Report the malaria status.
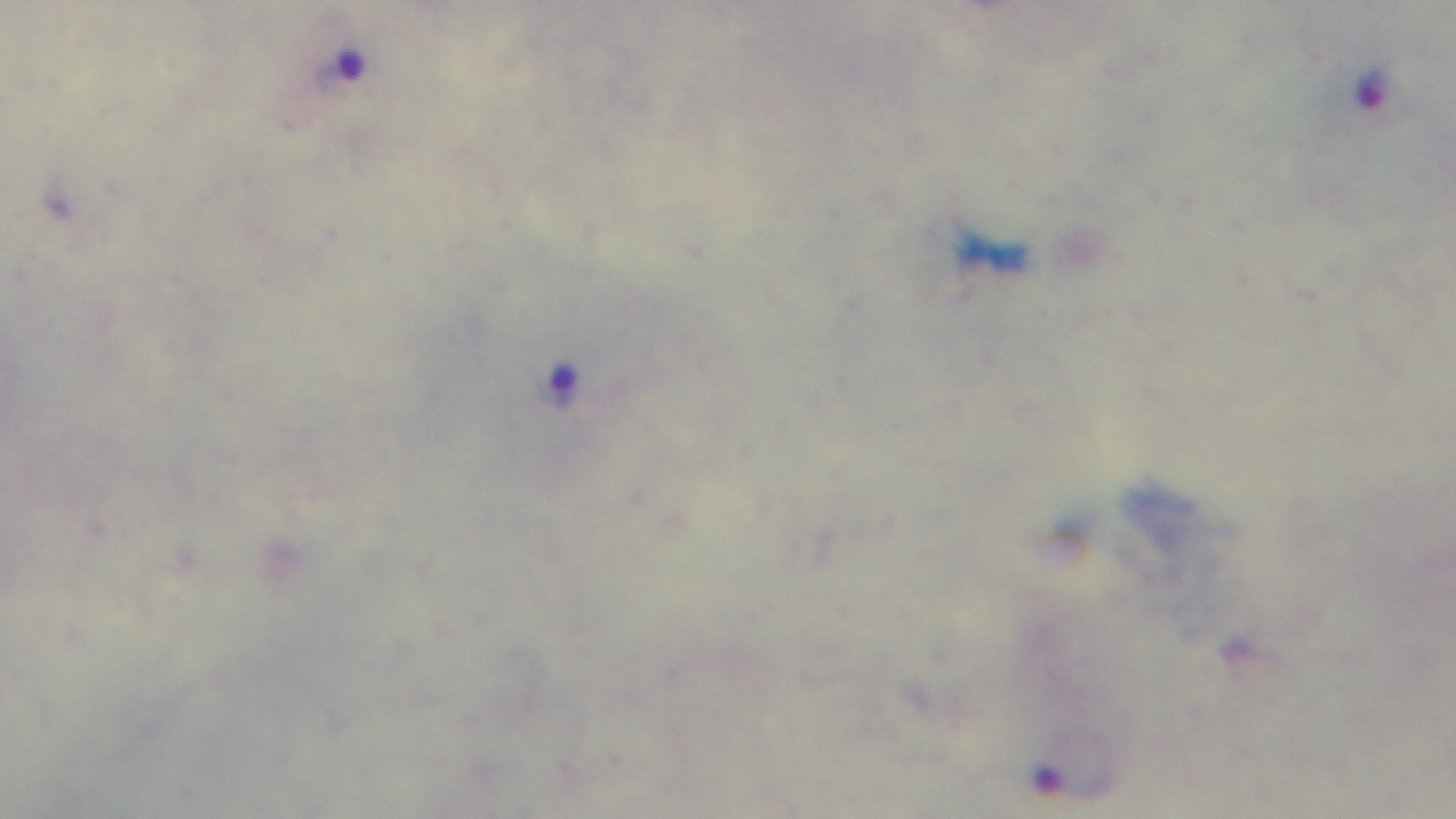

Positive.

field of view = one from the slide
stain = Giemsa
preparation = thick smear
modality = light microscopy
capture = mounted 4K digital camera
objective = 100x oil immersion